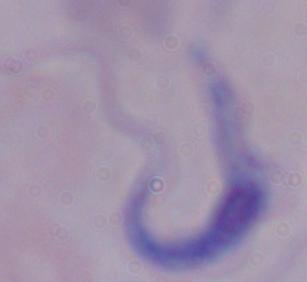

Summary:
  - Magnification: 1000x
  - Modality: micrograph
  - Identification: trypanosome